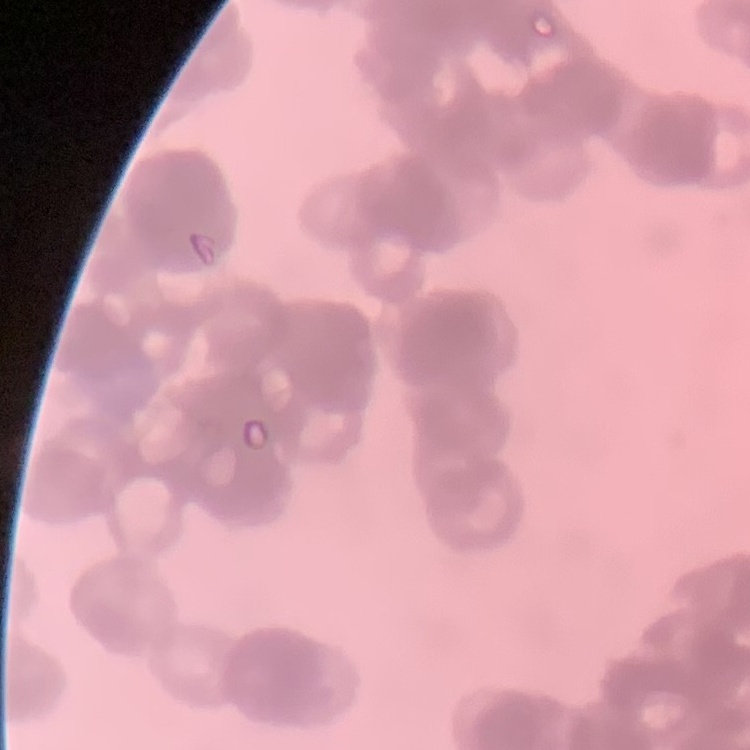

The red blood cells show rouleaux formation. Field's or Giemsa stain. Square crop of a larger photomicrograph. Thin blood film.